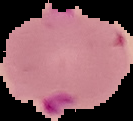
{
  "malaria_status": "parasitized",
  "image_size": "133×121 pixels",
  "preparation": "thin blood smear",
  "image_type": "cell region segmented out of the field of view; surrounding area masked to black"
}